Identify the cell.
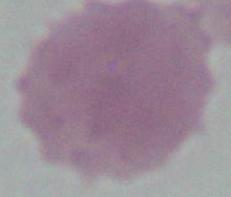
An erythrocyte.

Photomicrograph. Captured at 1000x magnification.